Assess this cell for malaria.
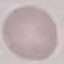

Uninfected.

Thin smear of blood. Automatically extracted cell patch, resized to 64 × 64 pixels. Photographed with a smartphone camera at the microscope eyepiece. Giemsa stain.